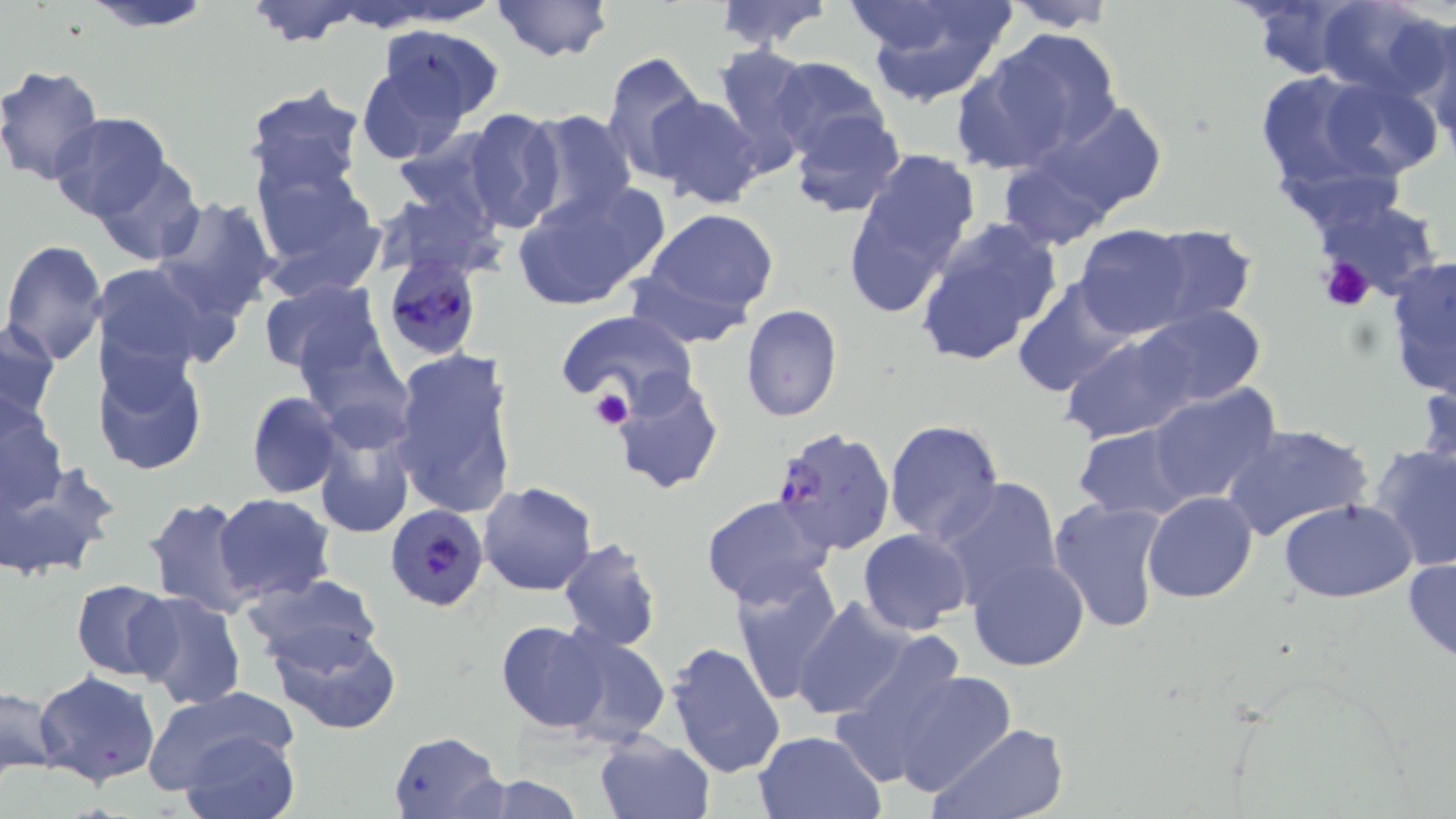

{
  "slide_level_diagnosis": "Plasmodium falciparum",
  "uninfected_red_blood_cell_locations": "approximate bounding boxes as named x1/y1/x2/y2 corners in pixels: (x1=74, y1=0, x2=221, y2=33), (x1=242, y1=0, x2=370, y2=48), (x1=490, y1=0, x2=614, y2=65), (x1=712, y1=0, x2=834, y2=51), (x1=855, y1=0, x2=1012, y2=105), (x1=999, y1=0, x2=1123, y2=32), (x1=1315, y1=0, x2=1447, y2=97), (x1=1237, y1=1, x2=1362, y2=81), (x1=1408, y1=18, x2=1456, y2=148), (x1=374, y1=26, x2=505, y2=126), (x1=986, y1=28, x2=1122, y2=149), (x1=714, y1=45, x2=820, y2=173), (x1=601, y1=51, x2=706, y2=183), (x1=950, y1=53, x2=1073, y2=174), (x1=356, y1=54, x2=477, y2=163), (x1=767, y1=56, x2=890, y2=162), (x1=0, y1=63, x2=106, y2=186), (x1=1250, y1=67, x2=1400, y2=201), (x1=1311, y1=73, x2=1445, y2=184), (x1=242, y1=84, x2=366, y2=198), (x1=645, y1=94, x2=766, y2=209), (x1=1029, y1=98, x2=1168, y2=220), (x1=464, y1=107, x2=567, y2=234), (x1=788, y1=108, x2=905, y2=219), (x1=520, y1=109, x2=637, y2=222), (x1=49, y1=112, x2=171, y2=224), (x1=842, y1=146, x2=980, y2=312), (x1=249, y1=152, x2=384, y2=293), (x1=997, y1=154, x2=1114, y2=252), (x1=91, y1=156, x2=204, y2=265), (x1=512, y1=181, x2=670, y2=312), (x1=1308, y1=195, x2=1444, y2=301), (x1=150, y1=196, x2=280, y2=322), (x1=641, y1=208, x2=780, y2=325), (x1=915, y1=216, x2=1065, y2=368), (x1=1074, y1=224, x2=1197, y2=340), (x1=1140, y1=224, x2=1260, y2=326), (x1=2, y1=240, x2=108, y2=366), (x1=1384, y1=256, x2=1456, y2=401), (x1=89, y1=262, x2=220, y2=378), (x1=258, y1=277, x2=385, y2=381), (x1=1013, y1=277, x2=1136, y2=396), (x1=739, y1=304, x2=842, y2=422), (x1=1133, y1=306, x2=1266, y2=410), (x1=555, y1=309, x2=696, y2=411), (x1=290, y1=311, x2=414, y2=442), (x1=1, y1=321, x2=60, y2=429), (x1=1056, y1=323, x2=1219, y2=448), (x1=94, y1=345, x2=207, y2=477), (x1=389, y1=348, x2=519, y2=520), (x1=1417, y1=370, x2=1456, y2=497), (x1=609, y1=371, x2=724, y2=496), (x1=1146, y1=382, x2=1282, y2=509), (x1=247, y1=392, x2=343, y2=498), (x1=0, y1=398, x2=67, y2=516), (x1=882, y1=419, x2=1004, y2=545), (x1=312, y1=420, x2=415, y2=539), (x1=1223, y1=423, x2=1374, y2=543), (x1=1072, y1=424, x2=1199, y2=522), (x1=1368, y1=443, x2=1456, y2=572), (x1=0, y1=457, x2=117, y2=580), (x1=938, y1=477, x2=1063, y2=605), (x1=478, y1=481, x2=598, y2=596), (x1=699, y1=492, x2=835, y2=609), (x1=1142, y1=492, x2=1257, y2=603), (x1=215, y1=493, x2=335, y2=603), (x1=143, y1=496, x2=259, y2=618), (x1=1047, y1=497, x2=1170, y2=635), (x1=1278, y1=499, x2=1417, y2=602), (x1=858, y1=528, x2=973, y2=635), (x1=557, y1=538, x2=662, y2=652), (x1=966, y1=556, x2=1088, y2=671), (x1=1402, y1=556, x2=1456, y2=666), (x1=732, y1=565, x2=844, y2=707), (x1=243, y1=574, x2=382, y2=672), (x1=71, y1=578, x2=176, y2=679), (x1=130, y1=591, x2=246, y2=710), (x1=791, y1=594, x2=915, y2=721), (x1=267, y1=620, x2=402, y2=736), (x1=495, y1=620, x2=613, y2=733), (x1=553, y1=630, x2=670, y2=748), (x1=662, y1=640, x2=785, y2=779), (x1=849, y1=649, x2=1011, y2=794), (x1=32, y1=671, x2=161, y2=787), (x1=0, y1=684, x2=63, y2=778), (x1=141, y1=686, x2=302, y2=803), (x1=926, y1=721, x2=1071, y2=819), (x1=753, y1=729, x2=885, y2=818), (x1=181, y1=730, x2=298, y2=819), (x1=387, y1=731, x2=506, y2=819), (x1=594, y1=735, x2=715, y2=819), (x1=473, y1=774, x2=588, y2=818)",
  "modality": "light microscopy",
  "stain": "May-Grünwald-Giemsa",
  "image_size": "1456×819 pixels",
  "preparation": "thin blood smear",
  "plasmodium_falciparum_infected_red_blood_cell_locations": "approximate bounding boxes as named x1/y1/x2/y2 corners in pixels: (x1=382, y1=254, x2=481, y2=360), (x1=769, y1=426, x2=896, y2=556), (x1=386, y1=503, x2=488, y2=611)",
  "magnification": "1000x",
  "field_of_view": "one of a larger specimen",
  "platelet_locations": "approximate bounding boxes as named x1/y1/x2/y2 corners in pixels: (x1=1318, y1=258, x2=1375, y2=314), (x1=591, y1=387, x2=633, y2=432)"
}